Give the extent of all white blood cells.
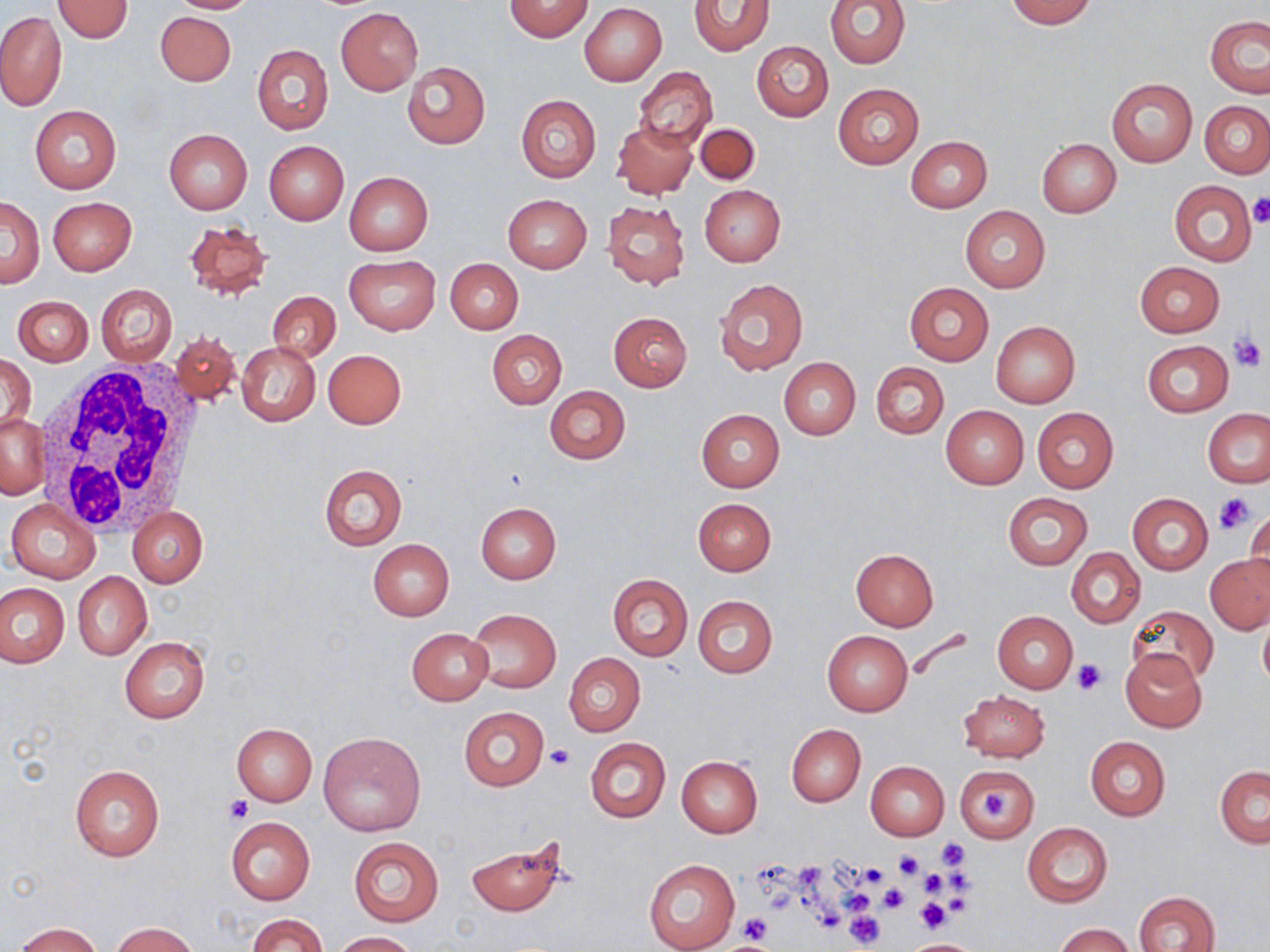
Approximate bounding boxes as [x1, y1, x2, y2] in pixels.
White blood cells: [33, 359, 204, 536].

slide_level_diagnosis: negative for blood parasites
uninfected_red_blood_cell_locations: 'approximate bounding boxes as [x1, y1, x2, y2] in pixels: [164, 0, 260, 14], [503, 0, 593, 42], [824, 0, 911, 68], [1004, 0, 1096, 28], [52, 1, 134, 43], [688, 1, 774, 55], [580, 4, 667, 85], [336, 7, 423, 96], [155, 11, 236, 86], [0, 12, 66, 112], [1205, 15, 1270, 98], [751, 41, 833, 122], [252, 44, 334, 135], [402, 62, 490, 149], [635, 68, 717, 148], [1106, 77, 1197, 166], [832, 83, 923, 169], [516, 94, 601, 182], [1200, 100, 1270, 179], [29, 105, 121, 193], [612, 120, 698, 198], [696, 124, 760, 184], [164, 129, 253, 214], [907, 136, 992, 213], [1037, 139, 1121, 217], [263, 140, 348, 225], [344, 171, 433, 256], [1169, 180, 1257, 267], [699, 185, 786, 266], [502, 193, 592, 273], [2, 197, 43, 288], [49, 197, 136, 276], [601, 199, 690, 290], [960, 205, 1050, 292], [182, 219, 274, 301], [345, 255, 440, 334], [445, 258, 523, 334], [1134, 261, 1224, 337], [714, 279, 808, 378], [904, 281, 993, 366], [96, 283, 177, 367], [268, 291, 341, 362], [13, 296, 93, 366], [608, 312, 692, 391], [991, 321, 1080, 407], [487, 329, 566, 409], [170, 332, 241, 405], [1142, 340, 1233, 417], [237, 342, 320, 425], [322, 349, 407, 428], [1, 354, 35, 434], [780, 358, 861, 440], [871, 362, 949, 439], [545, 385, 631, 464], [941, 406, 1028, 490], [1033, 408, 1119, 492], [696, 409, 785, 491], [1203, 409, 1270, 487], [1, 414, 50, 499], [319, 465, 407, 550], [1002, 492, 1092, 570], [1127, 493, 1213, 574], [693, 498, 775, 576], [6, 499, 100, 584], [476, 502, 562, 583], [128, 506, 208, 587], [1246, 506, 1270, 588], [368, 539, 454, 621], [1066, 548, 1146, 629], [851, 549, 938, 631], [1205, 553, 1270, 634], [72, 572, 152, 659], [608, 574, 693, 661], [0, 582, 69, 667], [693, 595, 777, 678], [1126, 605, 1219, 688], [1258, 606, 1270, 695], [467, 609, 561, 692], [993, 611, 1077, 693], [407, 628, 492, 705], [822, 630, 913, 716], [119, 638, 209, 723], [1121, 650, 1207, 731], [565, 653, 645, 736], [957, 690, 1050, 762], [459, 707, 549, 791], [231, 723, 317, 805], [786, 724, 866, 806], [318, 731, 426, 836], [1085, 736, 1170, 820], [585, 738, 671, 822], [676, 755, 762, 837], [865, 761, 950, 840], [69, 763, 165, 862], [956, 765, 1037, 842], [1215, 765, 1269, 847], [226, 817, 315, 904], [1022, 823, 1112, 908], [463, 836, 569, 916], [348, 837, 444, 927], [644, 858, 741, 952], [1133, 890, 1219, 952], [249, 914, 325, 952], [112, 921, 199, 952], [14, 922, 104, 951], [1055, 922, 1134, 952], [331, 931, 418, 951], [905, 939, 976, 951]'
stain: May-Grünwald-Giemsa
modality: light microscopy
platelet_locations: 'approximate bounding boxes as [x1, y1, x2, y2] in pixels: [1249, 193, 1270, 227], [1229, 334, 1267, 372], [1214, 492, 1255, 534], [1074, 659, 1107, 695], [547, 743, 574, 770], [225, 797, 254, 824], [935, 837, 970, 868], [893, 851, 924, 880], [859, 864, 891, 891], [918, 869, 949, 897], [878, 883, 908, 914], [915, 897, 952, 933], [845, 911, 885, 950], [741, 915, 774, 944]'
field_of_view: single
preparation: thin blood smear
image_size: 1270×952 pixels
magnification: 1000x